Outline each Plasmodium ovale-infected red blood cell.
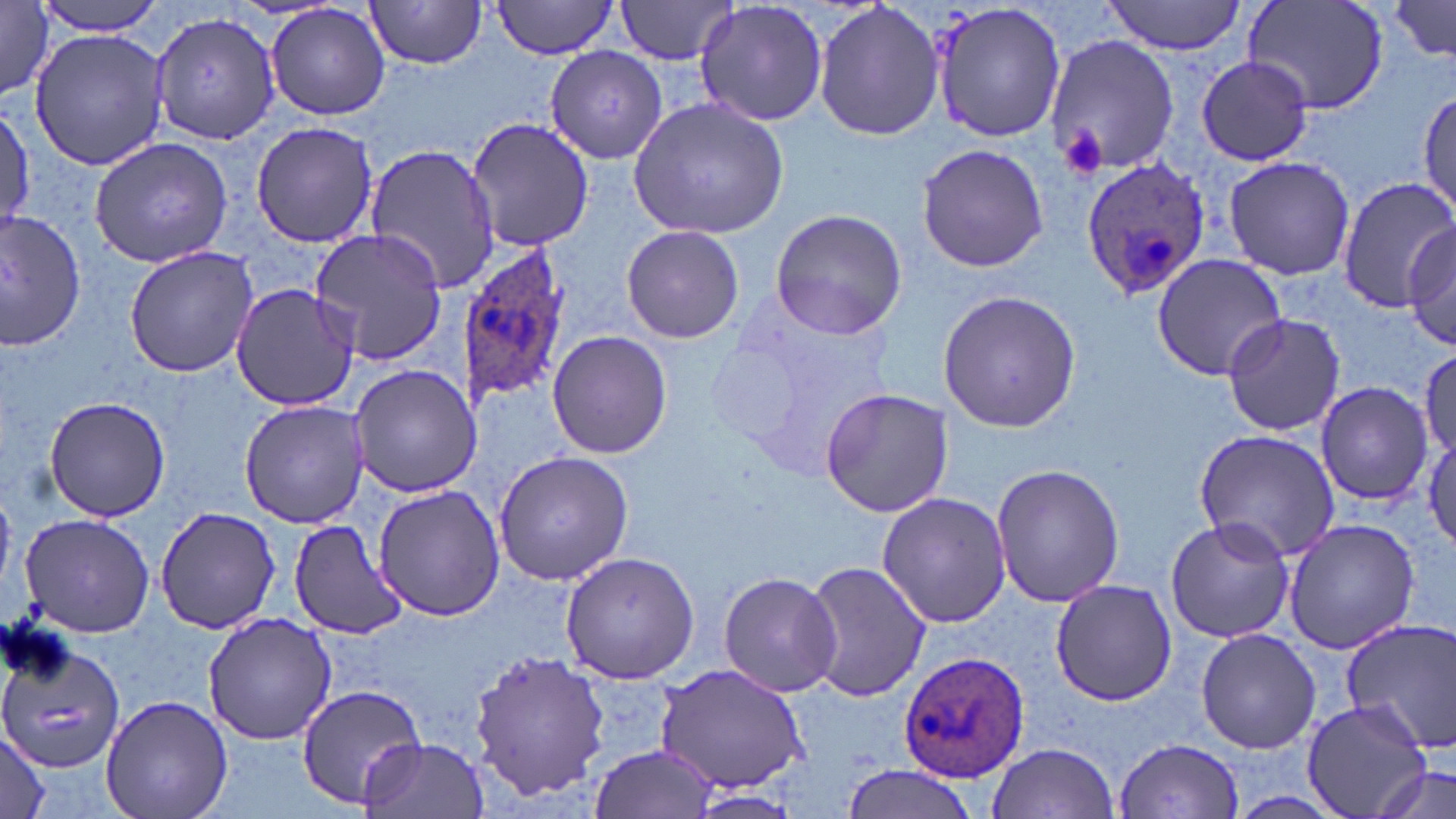

Approximate bounding boxes as (x1, y1, x2, y2) in pixels.
Plasmodium ovale-infected red blood cells: (1080, 157, 1211, 299), (458, 244, 572, 407), (900, 652, 1030, 781).

slide-level diagnosis = Plasmodium ovale
preparation = thin blood smear
modality = light microscopy
stain = May-Grünwald-Giemsa
field of view = single
magnification = 1000x
image size = 1456×819 pixels
uninfected red blood cell locations = approximate bounding boxes as (x1, y1, x2, y2) in pixels: (30, 0, 172, 37), (614, 0, 738, 65), (694, 0, 829, 128), (813, 0, 945, 142), (930, 0, 1067, 143), (1244, 0, 1389, 116), (1387, 0, 1456, 62), (364, 1, 487, 73), (489, 1, 622, 58), (1102, 1, 1248, 55), (0, 3, 55, 101), (267, 3, 392, 120), (149, 10, 281, 144), (30, 26, 167, 170), (1046, 34, 1180, 177), (546, 47, 667, 168), (1195, 55, 1315, 165), (1417, 85, 1454, 219), (629, 96, 788, 238), (0, 102, 33, 233), (466, 117, 592, 253), (250, 120, 379, 247), (88, 136, 233, 267), (916, 141, 1049, 273), (365, 143, 499, 292), (1222, 156, 1356, 281), (1335, 176, 1452, 314), (770, 206, 910, 339), (0, 209, 83, 350), (621, 224, 744, 344), (1404, 224, 1456, 354), (308, 229, 448, 363), (124, 245, 259, 377), (1153, 254, 1286, 381), (230, 283, 361, 411), (937, 290, 1084, 433), (710, 292, 891, 473), (1220, 311, 1346, 437), (547, 330, 672, 461), (1418, 348, 1456, 462), (348, 363, 479, 499), (1315, 382, 1432, 504), (819, 389, 953, 517), (44, 395, 171, 522), (238, 399, 370, 529), (1424, 426, 1456, 554), (1193, 429, 1341, 562), (495, 451, 632, 584), (992, 462, 1125, 608), (372, 486, 506, 622), (877, 493, 1011, 630), (156, 505, 279, 634), (17, 513, 155, 637), (1164, 517, 1295, 644), (1283, 518, 1419, 653), (289, 520, 411, 640), (558, 550, 701, 684), (801, 560, 930, 703), (717, 571, 843, 696), (1048, 577, 1180, 705), (203, 612, 336, 745), (1340, 617, 1456, 757), (1196, 628, 1322, 755), (0, 633, 127, 774), (468, 649, 609, 801), (654, 664, 813, 792), (295, 683, 428, 811), (101, 693, 232, 819), (1302, 699, 1432, 819), (0, 726, 51, 819), (360, 735, 489, 819), (1116, 738, 1243, 817), (987, 741, 1119, 819), (591, 744, 718, 819), (1371, 760, 1454, 819), (839, 763, 984, 819), (687, 790, 802, 819)
platelet locations = approximate bounding boxes as (x1, y1, x2, y2) in pixels: (1063, 125, 1106, 179)